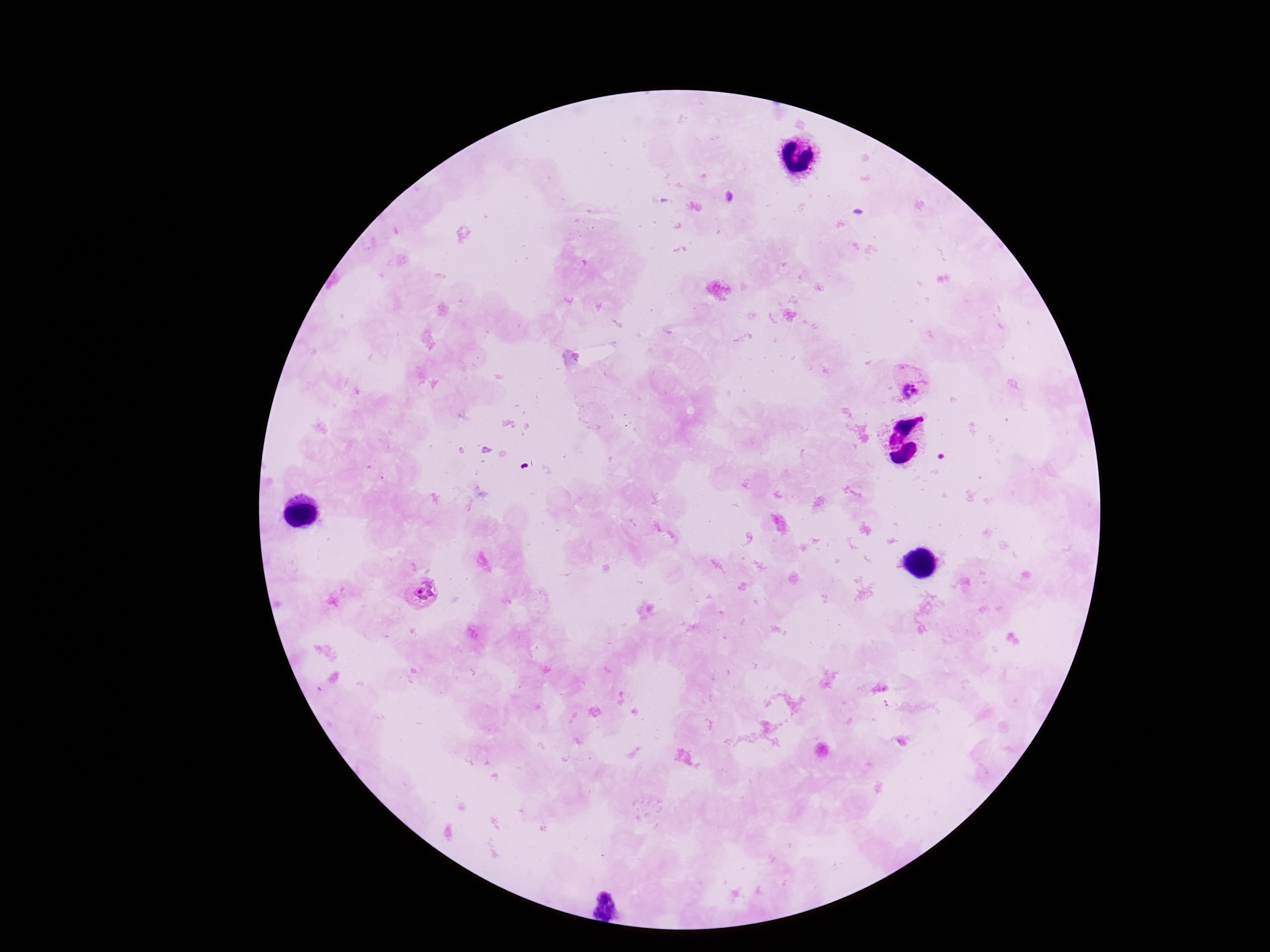
Approximate centers as (x, y) in pixels.
Summary:
  - Plasmodium parasite locations: (910, 382), (425, 594)
  - Stain: Giemsa
  - Capture: smartphone camera through the microscope eyepiece
  - Preparation: thick blood smear
  - Patient malaria status: positive
  - Image size: 1270×952 pixels
  - Magnification: 100x
  - Field of view: single